Give the preparation type.
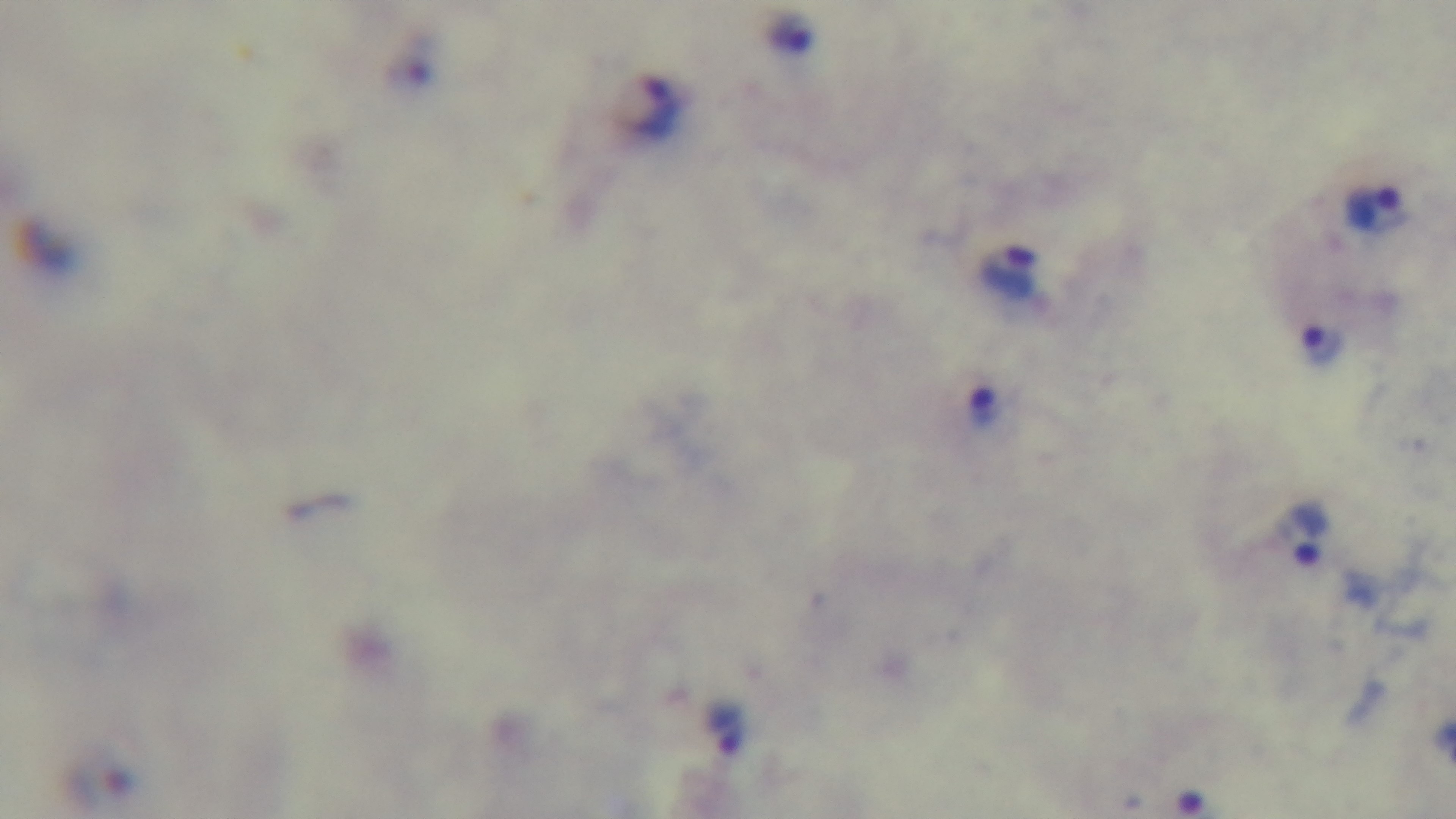

A thick smear.

Summary:
  - Capture: mounted 4K digital camera
  - Malaria status: positive
  - Field of view: one from the slide
  - Stain: Giemsa
  - Objective: 100x oil immersion
  - Modality: light microscopy